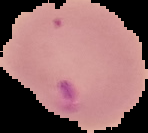
Summary:
  - Malaria status: parasitized
  - Image size: 148×133 pixels
  - Preparation: thin blood smear
  - Image type: segmented cell region with the area outside set to black